Locate every Plasmodium parasite and every leukocyte.
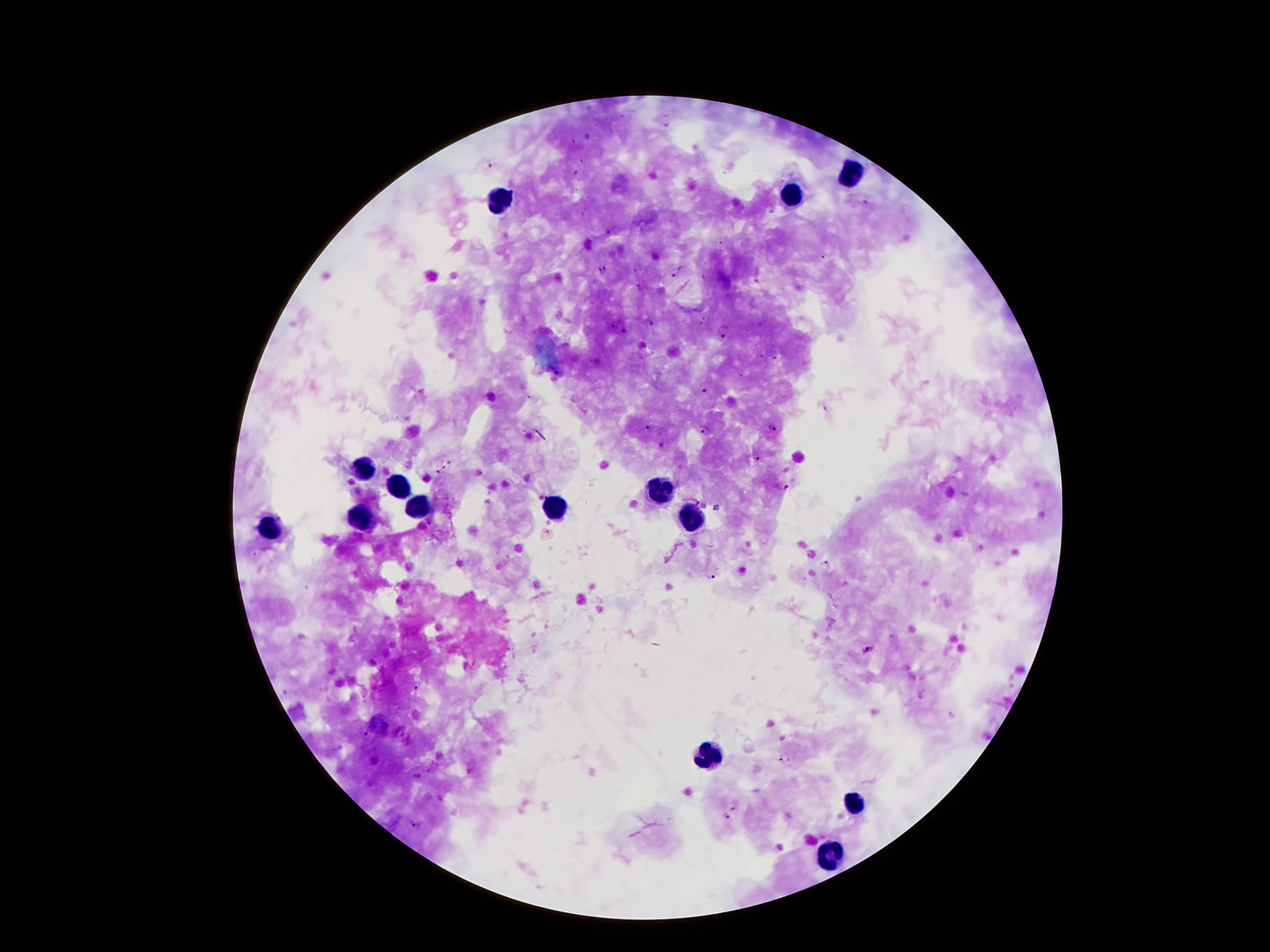

Approximate centers as {x, y} in pixels.
Plasmodium parasites: {491, 164}, {866, 201}, {611, 229}, {717, 242}, {826, 258}, {602, 270}, {676, 272}, {651, 322}, {723, 332}, {762, 356}, {775, 358}, {742, 375}, {705, 391}, {648, 428}, {772, 428}, {705, 432}, {662, 445}, {757, 459}, {450, 463}, {443, 468}, {437, 472}, {786, 488}, {697, 501}, {548, 531}, {825, 563}, {711, 576}, {868, 650}, {416, 686}, {364, 735}, {785, 758}, {733, 807}, {725, 816}, {409, 825}.
Leukocytes: {851, 173}, {790, 196}, {496, 201}, {363, 469}, {399, 489}, {658, 491}, {424, 508}, {551, 510}, {692, 517}, {363, 519}, {272, 530}, {705, 755}, {853, 807}, {830, 853}.

Summary:
  - Magnification: 100x
  - Patient malaria status: positive for Plasmodium falciparum
  - Stain: Giemsa
  - Field of view: single
  - Preparation: thick blood film
  - Image size: 1270×952 pixels
  - Capture: smartphone camera through the microscope eyepiece